Classify this cell by malaria status.
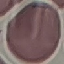

It is uninfected.

Summary:
  - Image type: automatically extracted cell patch, resized to 64 × 64 pixels
  - Capture: smartphone through the microscope eyepiece
  - Stain: Giemsa
  - Preparation: thin smear